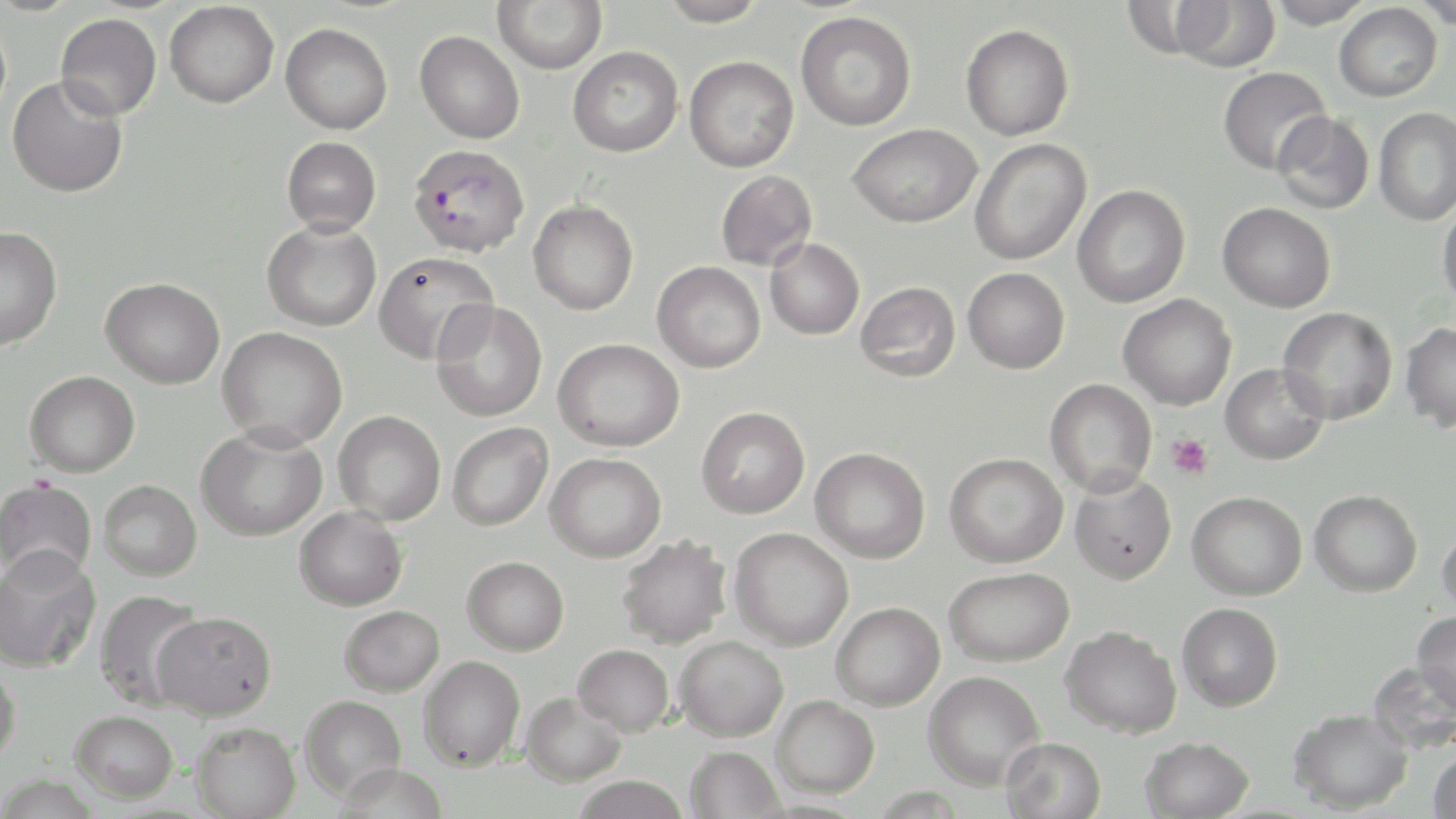

Approximate bounding boxes as (x1, y1, x2, y2) in pixels. Plasmodium falciparum-infected red blood cell locations: (408, 143, 529, 257). Platelet locations: (1166, 432, 1214, 479). Uninfected red blood cell locations: (493, 0, 608, 74), (657, 0, 768, 27), (1266, 0, 1375, 29), (1414, 0, 1456, 29), (165, 1, 279, 108), (1170, 1, 1280, 72), (1334, 3, 1442, 102), (795, 11, 916, 131), (55, 13, 162, 120), (280, 22, 393, 134), (960, 23, 1074, 141), (415, 31, 525, 143), (568, 46, 683, 157), (684, 55, 799, 172), (1218, 66, 1333, 175), (7, 76, 128, 198), (1373, 107, 1456, 225), (1272, 112, 1374, 214), (847, 123, 981, 228), (282, 136, 381, 235), (969, 139, 1091, 266), (716, 170, 817, 271), (1072, 184, 1190, 308), (528, 199, 638, 315), (1437, 201, 1456, 309), (1217, 202, 1335, 312), (262, 219, 381, 332), (0, 226, 62, 351), (765, 239, 864, 340), (373, 251, 499, 365), (652, 261, 765, 373), (963, 267, 1070, 373), (101, 277, 225, 388), (856, 281, 961, 381), (1118, 293, 1236, 410), (431, 299, 547, 422), (1278, 307, 1397, 424), (1400, 322, 1456, 432), (217, 326, 348, 450), (553, 338, 684, 451), (1220, 363, 1330, 465), (25, 370, 140, 477), (1045, 378, 1157, 497), (696, 406, 810, 518), (334, 410, 446, 525), (447, 422, 553, 531), (196, 424, 327, 541), (810, 447, 931, 563), (545, 452, 666, 562), (944, 453, 1068, 568), (1069, 473, 1176, 585), (0, 479, 95, 583), (99, 480, 202, 580), (1309, 489, 1422, 596), (1187, 490, 1307, 600), (295, 506, 407, 611), (1437, 521, 1456, 620), (728, 528, 854, 650), (616, 534, 732, 649), (0, 547, 101, 672), (462, 556, 569, 655), (944, 567, 1074, 666), (94, 589, 208, 709), (831, 602, 945, 710), (1177, 602, 1283, 711), (339, 605, 444, 696), (1412, 610, 1456, 712), (150, 611, 277, 720), (1060, 625, 1182, 737), (674, 636, 789, 741), (573, 644, 674, 735), (419, 655, 525, 771), (0, 659, 22, 767), (1368, 660, 1456, 755), (923, 670, 1045, 791), (520, 691, 627, 786), (300, 694, 406, 800), (772, 694, 879, 797), (1288, 708, 1413, 814), (71, 710, 178, 803), (190, 721, 301, 819), (1000, 736, 1107, 819), (1140, 736, 1254, 819), (685, 746, 785, 819), (1428, 746, 1456, 818), (334, 763, 449, 819), (570, 776, 691, 819). Slide-level diagnosis: Plasmodium falciparum. Image is 1456×819 pixels. 1000x magnification. Light microscopy. Thin blood film. May-Grünwald-Giemsa stain. One field of a larger specimen.